Give the position of every malaria parasite and every leukocyte.
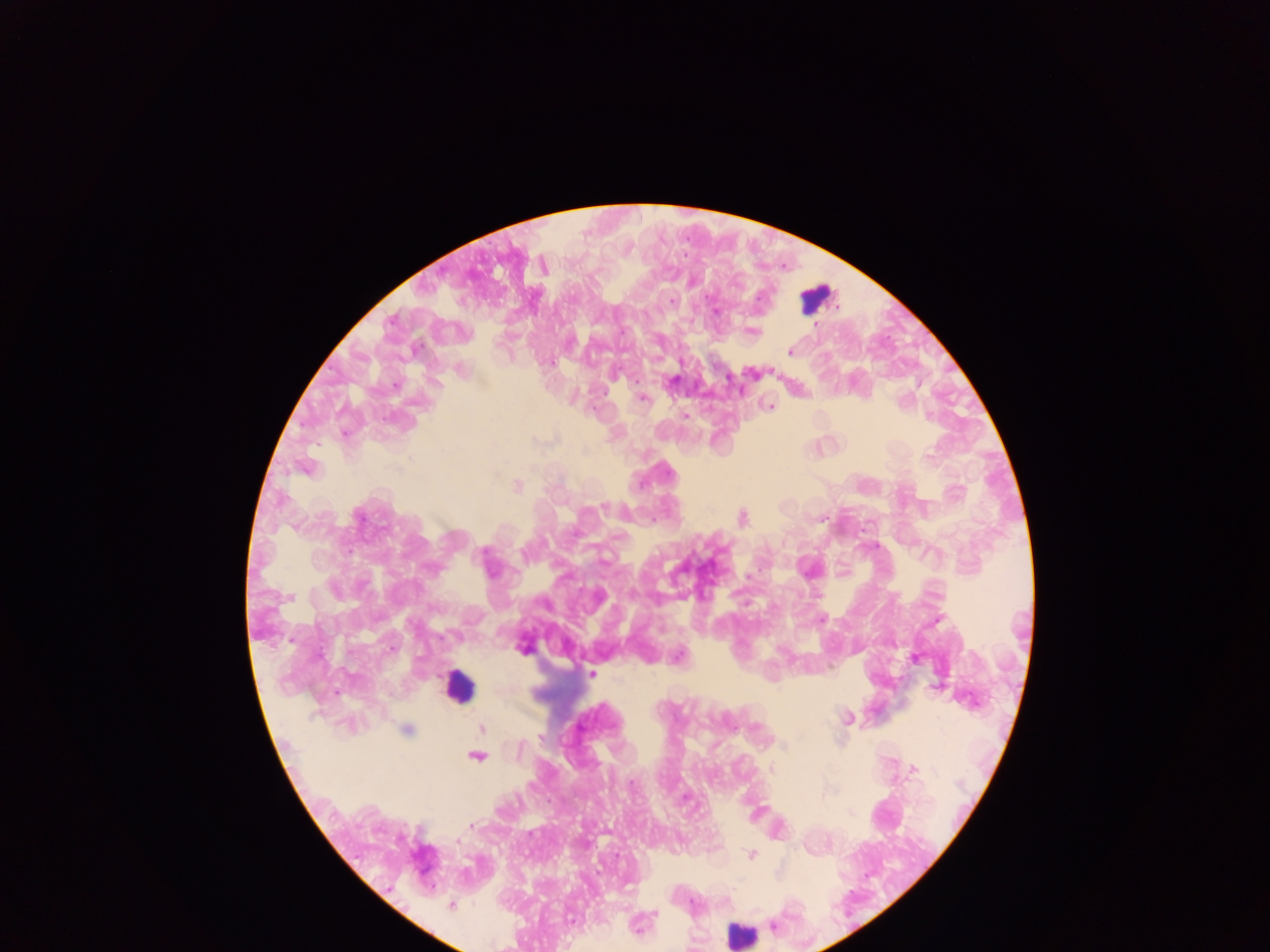

Approximate centers as [x, y] in pixels.
Malaria parasites: [671, 301], [716, 312], [815, 324], [753, 332], [790, 351], [551, 362], [672, 381], [396, 386], [642, 398], [771, 406], [685, 415], [929, 417], [584, 450], [518, 486], [604, 506], [359, 517], [743, 517], [821, 519], [483, 553], [821, 619], [524, 649], [392, 650], [680, 656], [592, 674], [846, 718], [482, 729], [406, 730], [540, 737], [783, 747], [519, 749], [477, 756], [772, 770], [914, 770], [632, 782], [471, 826], [456, 841], [617, 855], [751, 855], [450, 905], [655, 913], [773, 925].
Leukocytes: [816, 296], [457, 687], [740, 933].

{
  "preparation": "thick blood film",
  "capture": "mobile-phone photograph through a microscope",
  "field_of_view": "single",
  "country": "Ghana",
  "image_size": "1270×952 pixels"
}